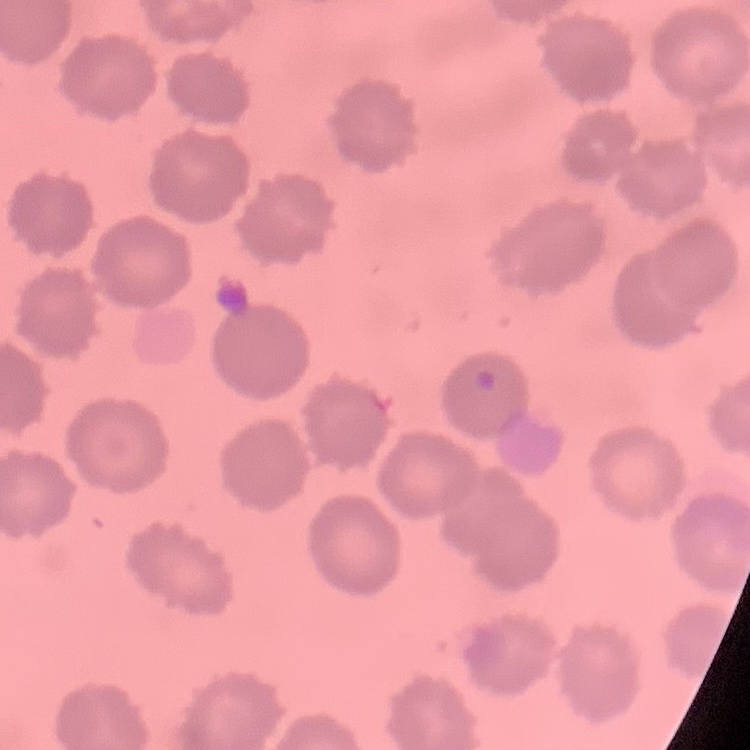

erythrocyte morphology = no rouleaux formation
stain = Field's or Giemsa
image type = square crop of a larger photomicrograph
preparation = thin blood film